State which parasite is depicted.
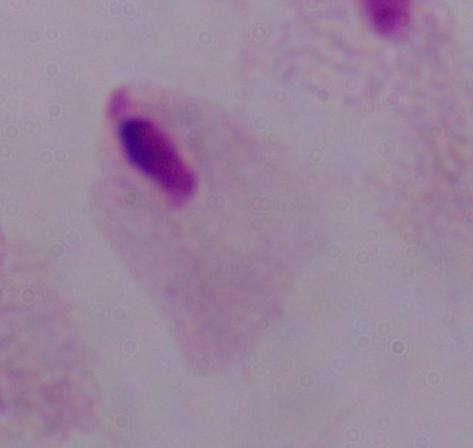
A trichomonad.

Summary:
  - Magnification: 1000x
  - Modality: photomicrograph